Identify the cell.
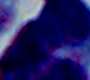
A leukocyte.

1000x magnification. Micrograph.